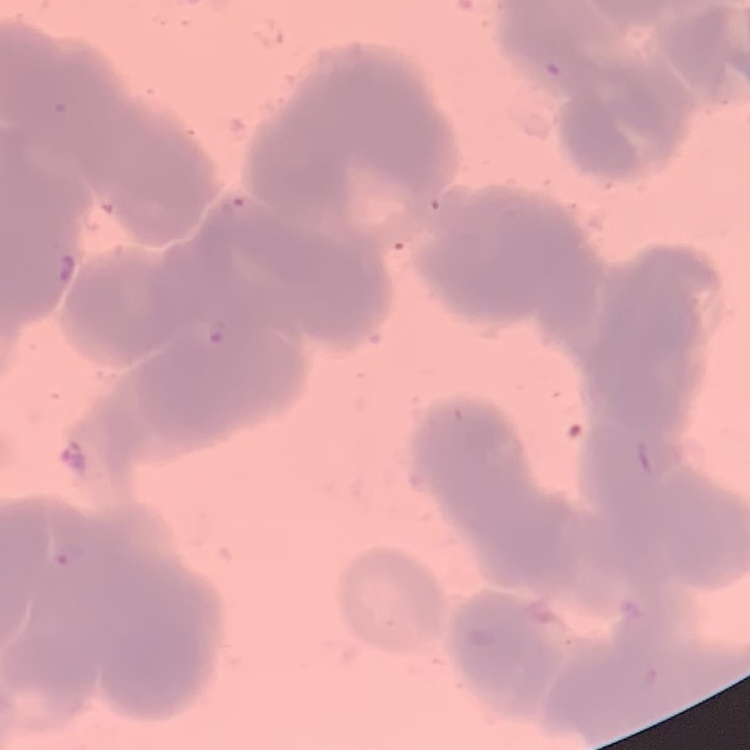

The erythrocytes show rouleaux formation. One tile cut from a larger photomicrograph. Thin blood film. Stained with either Field's or Giemsa.